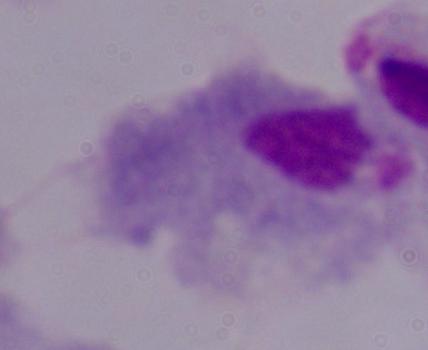

{
  "magnification": "1000x",
  "identification": "trichomonad",
  "modality": "photomicrograph"
}